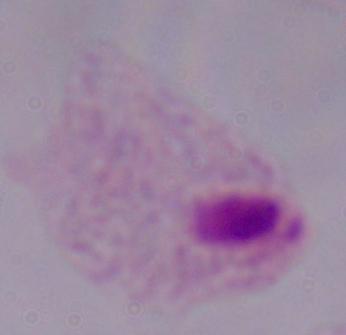

Summary:
  - Modality: photomicrograph
  - Identification: trichomonad
  - Magnification: 1000x